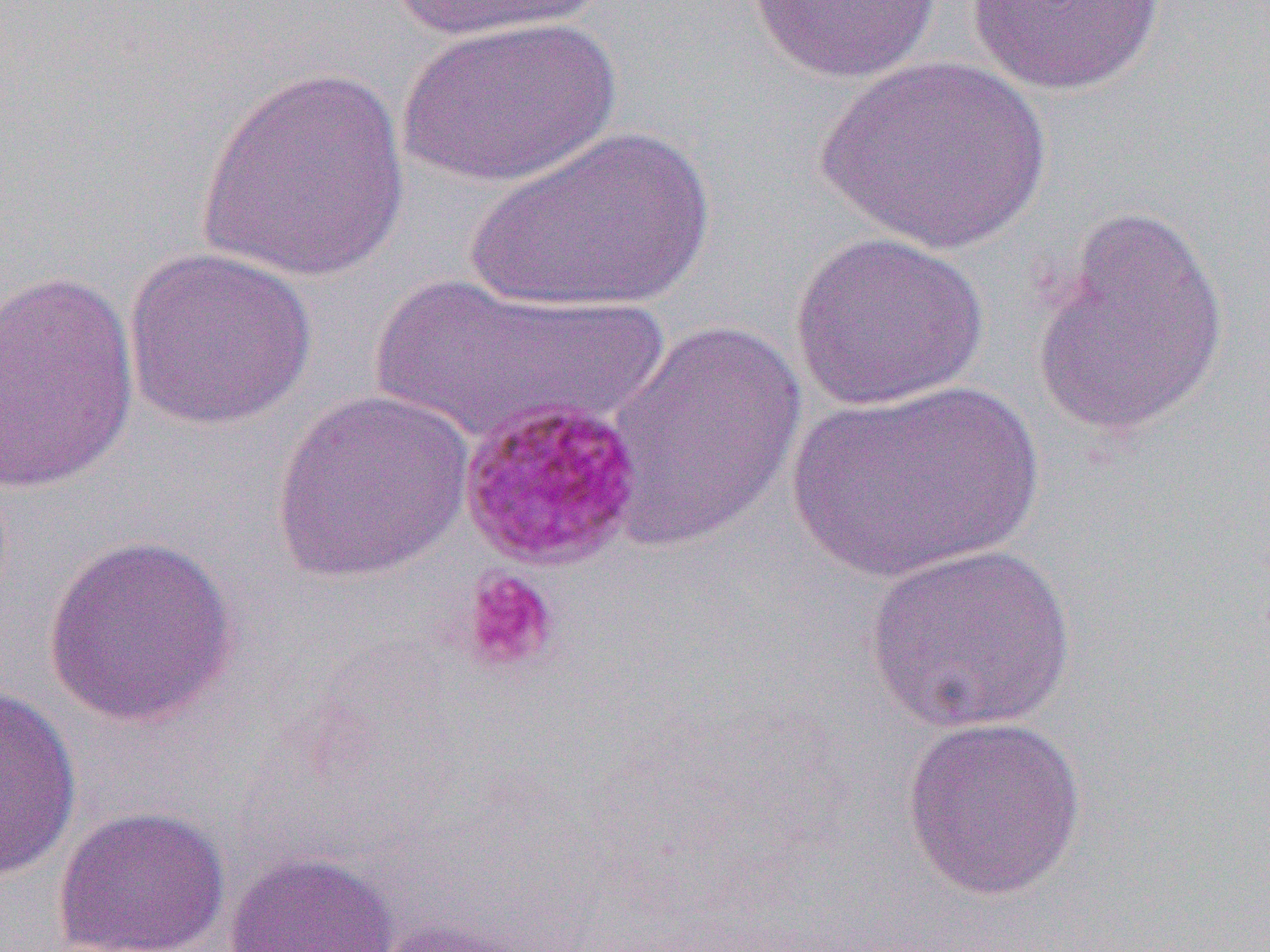 Approximate bounding boxes as [x1, y1, x2, y2] in pixels. Platelet locations (subset): [459, 568, 561, 675]. Uninfected red blood cell locations: [385, 0, 609, 45], [746, 1, 943, 84], [967, 1, 1167, 97], [398, 16, 621, 190], [817, 54, 1053, 255], [195, 65, 409, 284], [461, 125, 718, 315], [1029, 205, 1229, 438], [789, 231, 990, 412], [122, 246, 317, 431], [1, 268, 140, 497], [372, 273, 653, 448], [605, 318, 808, 552], [786, 379, 1043, 584], [270, 389, 476, 584], [42, 532, 241, 728], [862, 540, 1079, 736], [0, 682, 83, 888], [899, 714, 1088, 901], [52, 805, 232, 952], [224, 850, 399, 952], [362, 916, 543, 952]. Slide-level diagnosis: Plasmodium malariae. Single field of view. 1000x magnification. Optical microscopy. Image is 1270×952 pixels. Thin blood film.